Identify the parasite.
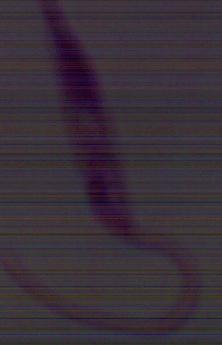
Leishmania.

1000x magnification. Micrograph.